Locate every blood parasite and identify its species.
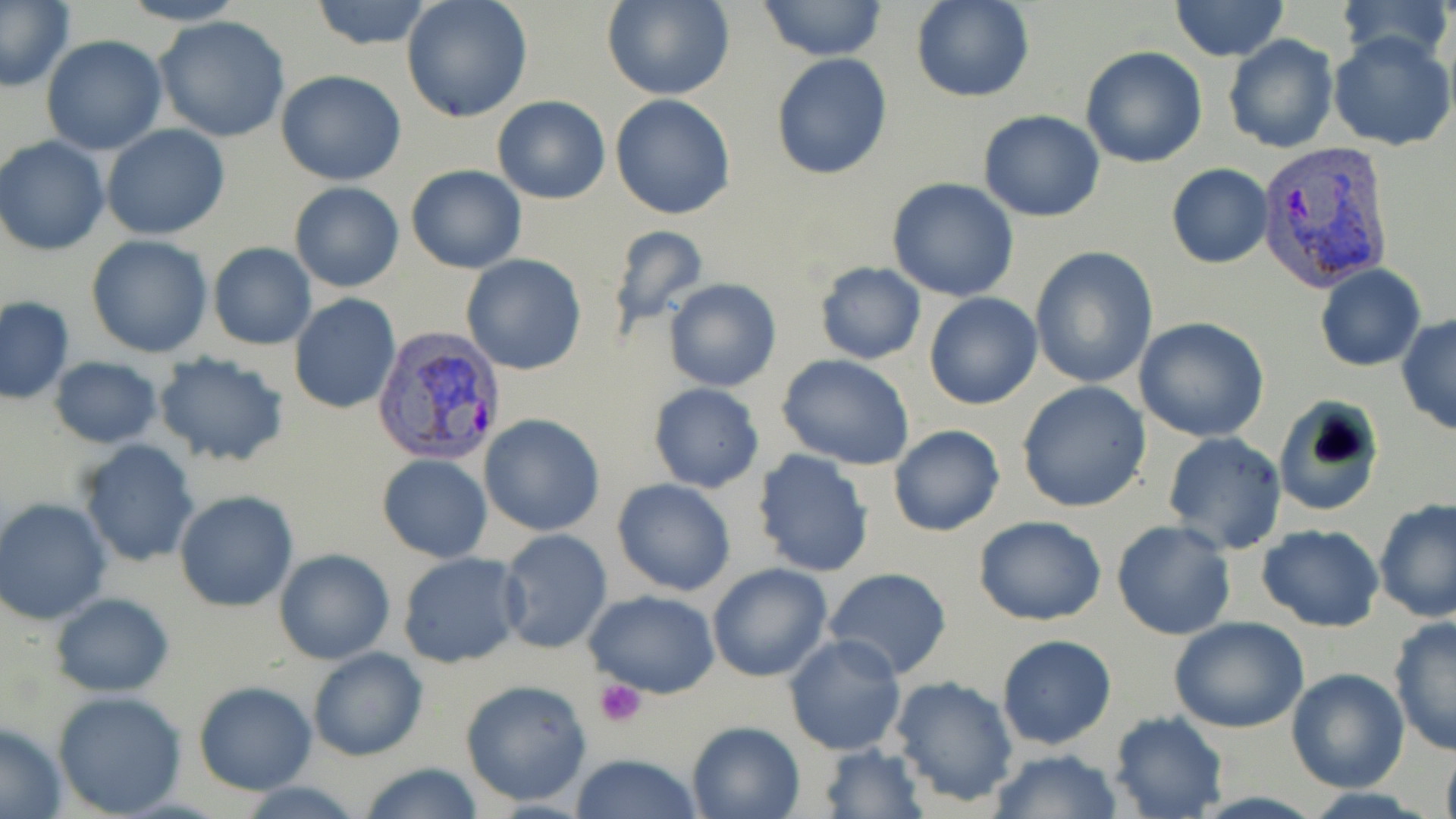
Approximate bounding boxes as (x1,y1)-(x2,y2) corner pairs in pixels.
Plasmodium vivax-infected red blood cells: (1256,140)-(1393,292), (372,327)-(507,468).
No Plasmodium falciparum, Plasmodium ovale, Plasmodium malariae, Babesia divergens, or Trypanosoma brucei observed.

slide-level diagnosis = Plasmodium vivax
image size = 1456×819 pixels
modality = light microscopy
preparation = thin blood film
magnification = 1000x
stain = May-Grünwald-Giemsa
field of view = single
platelet locations = approximate bounding boxes as (x1,y1)-(x2,y2) corner pairs in pixels: (594,679)-(647,727)
uninfected red blood cell locations = approximate bounding boxes as (x1,y1)-(x2,y2) corner pairs in pixels: (2,0)-(73,89), (117,0)-(248,26), (307,0)-(436,50), (401,0)-(532,121), (1170,0)-(1290,63), (1336,0)-(1454,67), (603,1)-(732,101), (910,1)-(1034,104), (755,2)-(890,60), (153,15)-(290,143), (1223,33)-(1339,154), (1328,33)-(1455,151), (40,36)-(168,156), (1081,46)-(1206,168), (771,53)-(893,180), (276,71)-(406,186), (611,93)-(735,219), (492,94)-(611,204), (978,111)-(1105,222), (102,124)-(231,240), (0,136)-(109,255), (1166,163)-(1273,268), (406,164)-(526,274), (886,179)-(1020,301), (289,182)-(405,293), (604,225)-(711,335), (84,235)-(214,358), (208,244)-(316,350), (1029,246)-(1160,388), (461,254)-(585,375), (813,261)-(926,365), (1314,265)-(1426,371), (664,278)-(781,392), (923,292)-(1042,410), (289,294)-(400,415), (1,297)-(74,405), (1397,313)-(1456,437), (1134,317)-(1272,442), (153,350)-(292,468), (775,355)-(918,471), (50,357)-(162,448), (1016,380)-(1152,514), (648,383)-(764,492), (1276,397)-(1385,517), (478,414)-(605,536), (888,424)-(1005,538), (1162,432)-(1288,556), (76,439)-(200,569), (752,451)-(875,577), (376,455)-(492,562), (612,478)-(736,598), (174,492)-(298,611), (1,497)-(115,625), (1374,499)-(1455,625), (973,515)-(1107,626), (1111,520)-(1236,640), (1257,525)-(1385,632), (496,529)-(612,654), (274,549)-(395,663), (398,552)-(528,670), (706,562)-(834,682), (823,567)-(953,680), (583,590)-(720,698), (50,592)-(174,697), (1170,618)-(1310,733), (1388,619)-(1455,757), (784,635)-(907,756), (996,635)-(1118,752), (307,647)-(428,762), (1284,668)-(1410,795), (890,675)-(1020,808), (460,679)-(593,807), (191,680)-(318,796), (52,690)-(188,816), (1108,711)-(1228,819), (687,720)-(806,819), (0,724)-(68,819), (818,743)-(928,818), (1440,745)-(1456,819), (987,749)-(1123,819), (570,752)-(704,819), (356,762)-(485,819)